Report the malaria status.
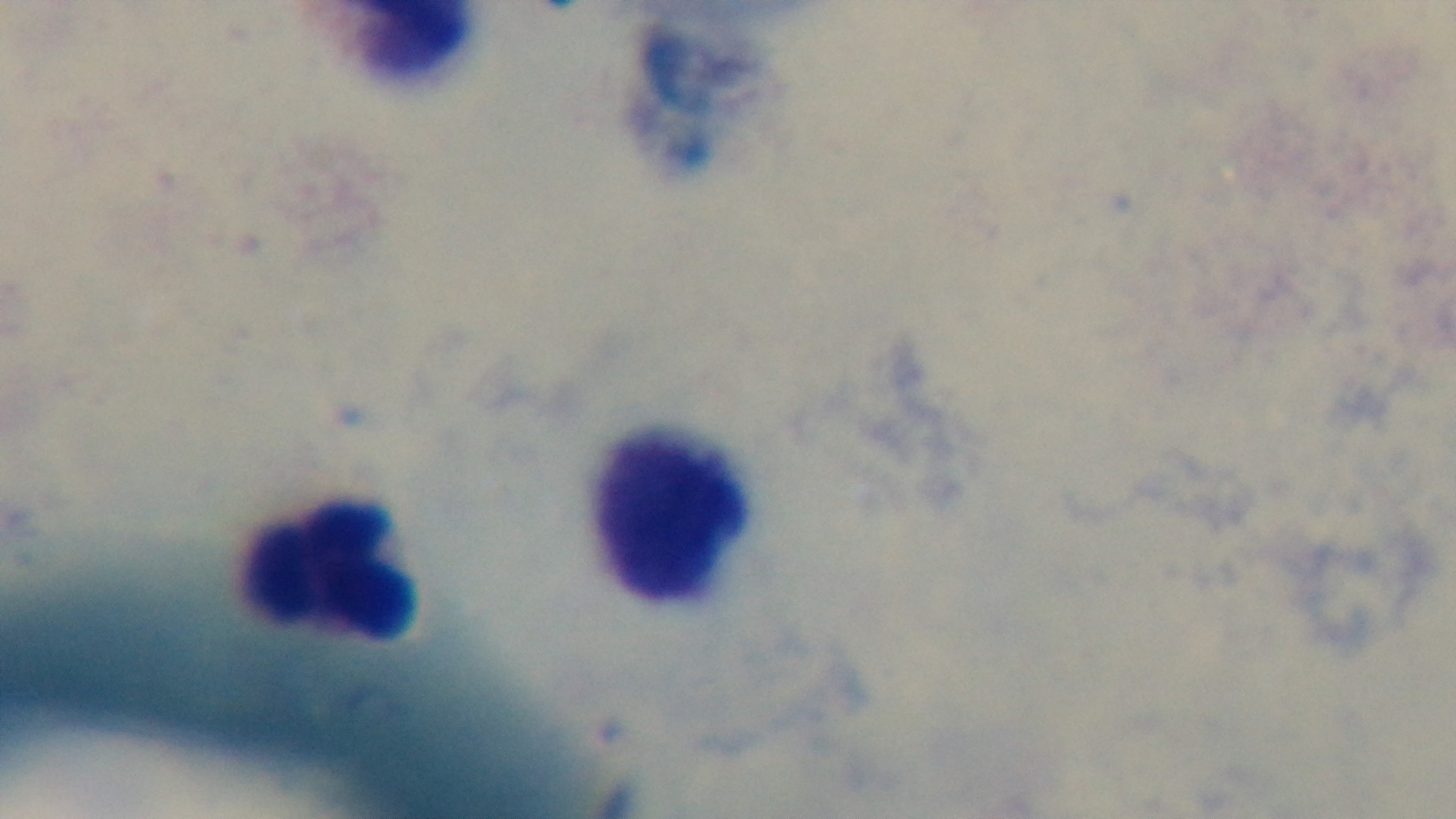

Uninfected.

Summary:
  - Preparation: thick smear
  - Objective: 100x oil immersion
  - Stain: Giemsa
  - Modality: light microscopy
  - Capture: mounted 4K digital camera
  - Field of view: one from the slide